Assess for malaria.
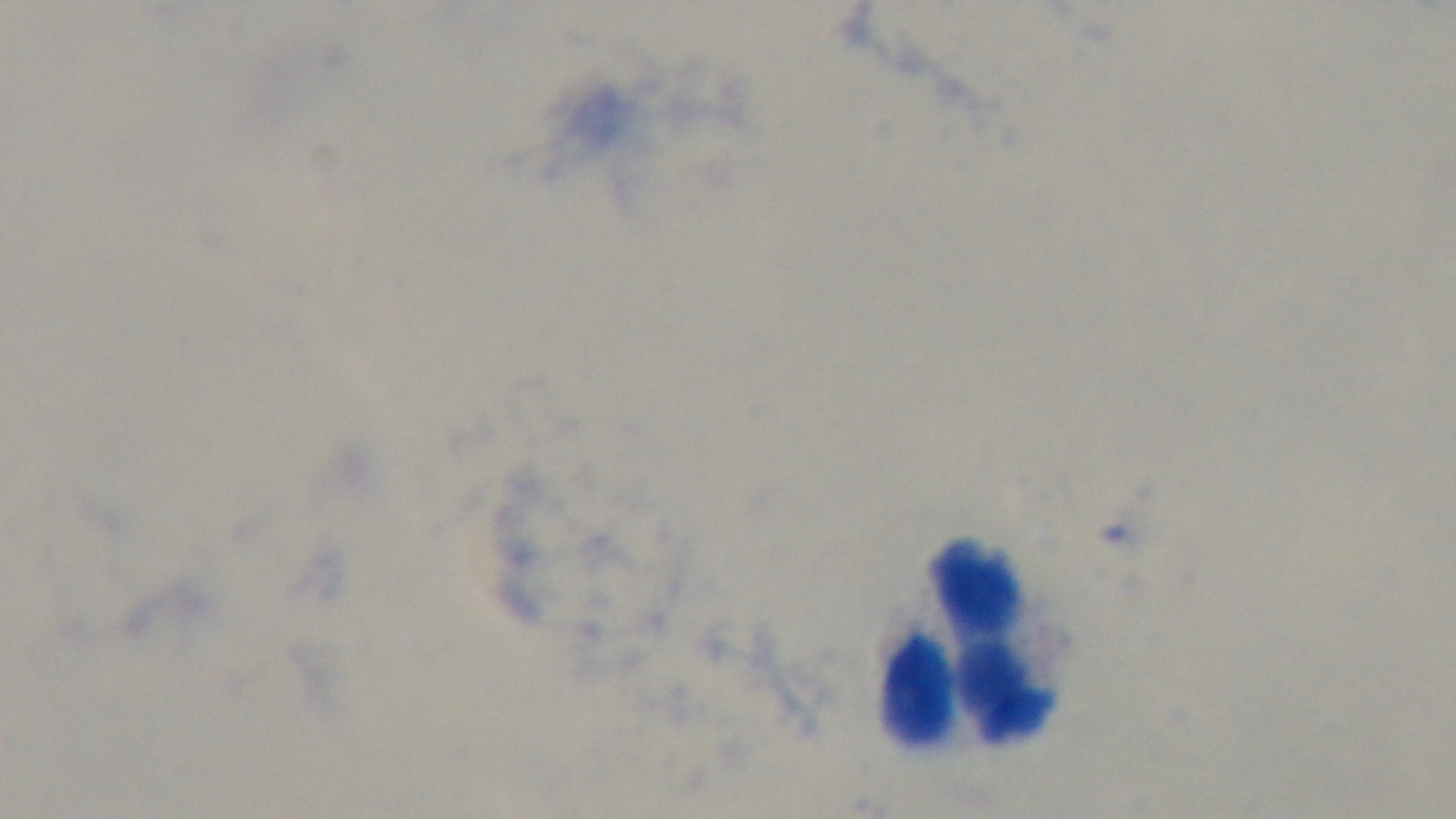

Negative.

modality = light microscopy
field of view = one from the slide
stain = Giemsa
capture = mounted 4K digital camera
objective = 100x oil immersion
preparation = thick smear